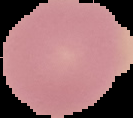
Summary:
  - Result: negative for Plasmodium parasites
  - Preparation: thin blood film
  - Image type: segmented cell region on a black background
  - Image size: 133×118 pixels